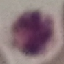

result = no malaria parasites detected
image type = cell patch, automatically extracted from a larger field of view and resized to 64 × 64 pixels
preparation = thin blood film
stain = Giemsa
capture = smartphone camera at the microscope eyepiece